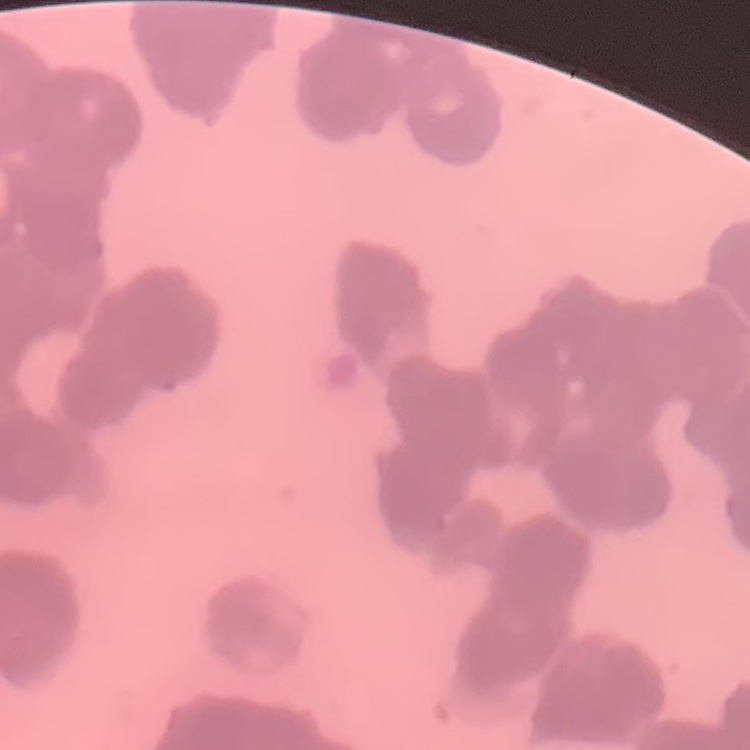
Summary:
  - Erythrocyte morphology: rouleaux formation
  - Stain: Field's or Giemsa
  - Image type: one tile cut from a larger photomicrograph
  - Preparation: thin blood film